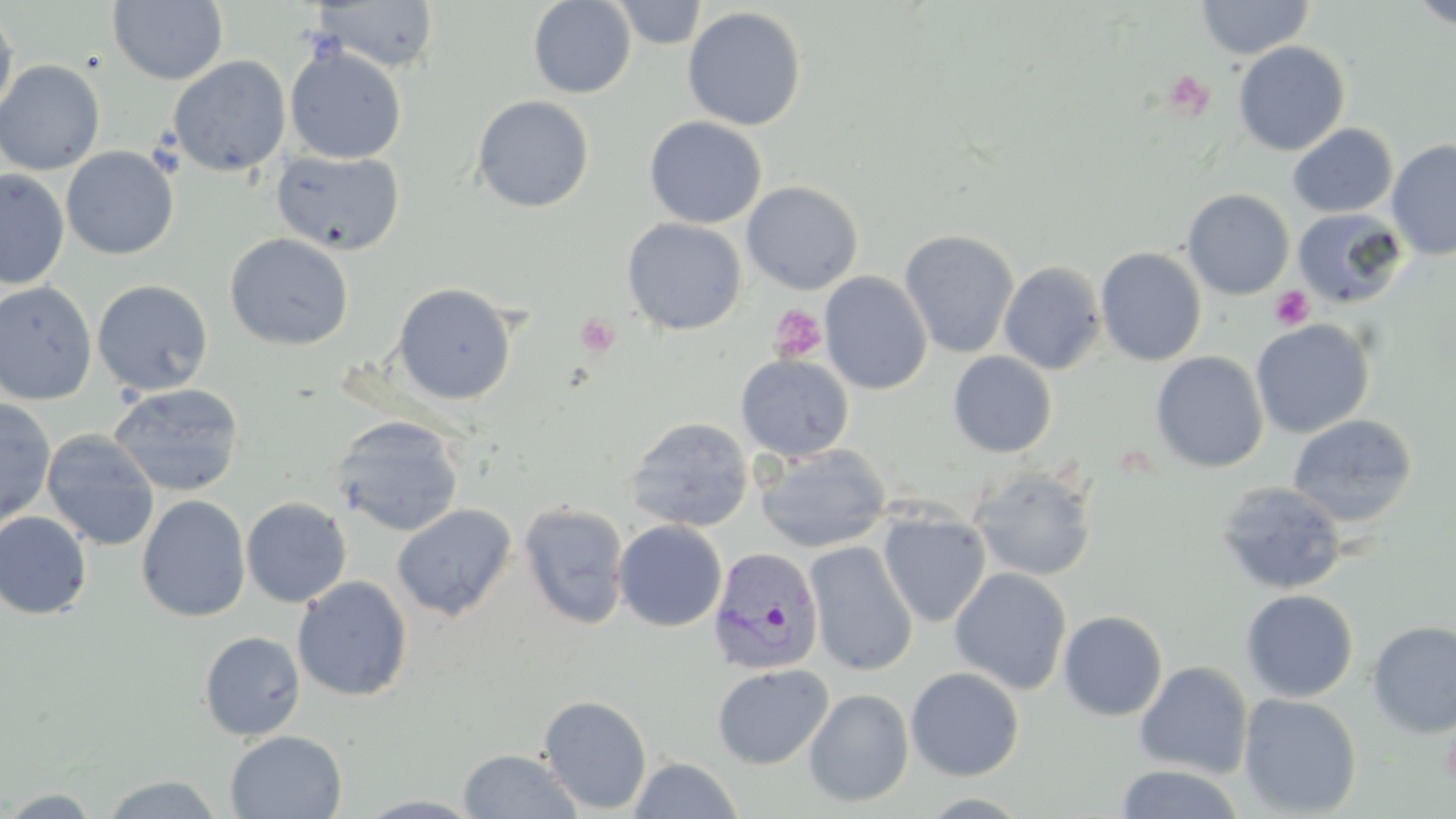
Approximate bounding boxes as [x1, y1, x2, y2] in pixels. Plasmodium vivax-infected red blood cell locations: [707, 546, 824, 675]. Uninfected red blood cell locations: [611, 0, 708, 49], [1195, 0, 1313, 59], [1407, 0, 1456, 31], [107, 1, 229, 85], [311, 1, 440, 74], [528, 1, 636, 98], [0, 5, 18, 123], [683, 6, 806, 131], [1232, 41, 1350, 156], [285, 45, 407, 164], [168, 56, 291, 177], [0, 59, 105, 175], [471, 95, 594, 213], [644, 116, 767, 228], [1287, 123, 1397, 218], [1386, 139, 1456, 261], [61, 146, 179, 260], [271, 149, 405, 256], [0, 169, 69, 289], [741, 180, 864, 295], [1182, 189, 1295, 300], [1292, 208, 1408, 308], [621, 218, 747, 335], [899, 229, 1019, 359], [224, 233, 354, 351], [1095, 246, 1207, 366], [999, 262, 1106, 374], [820, 271, 933, 395], [91, 279, 213, 396], [0, 281, 97, 405], [392, 282, 516, 405], [1250, 319, 1375, 438], [948, 351, 1057, 457], [1150, 351, 1268, 472], [735, 353, 855, 462], [108, 383, 246, 497], [0, 399, 56, 528], [1287, 414, 1418, 527], [331, 415, 465, 537], [624, 416, 755, 533], [41, 430, 160, 551], [755, 443, 891, 553], [968, 466, 1098, 582], [1215, 481, 1349, 595], [136, 494, 251, 622], [241, 497, 352, 608], [518, 502, 630, 629], [392, 503, 516, 621], [878, 509, 991, 627], [0, 511, 93, 620], [613, 520, 727, 632], [805, 540, 918, 676], [949, 567, 1072, 694], [292, 576, 413, 702], [1240, 589, 1358, 702], [1058, 610, 1168, 721], [1367, 621, 1456, 738], [199, 631, 306, 741], [1134, 661, 1253, 779], [712, 663, 833, 769], [905, 666, 1024, 781], [804, 688, 914, 807], [1237, 693, 1362, 818], [538, 695, 652, 814], [225, 730, 347, 818], [457, 748, 583, 819], [629, 756, 743, 818], [1113, 764, 1244, 819], [99, 774, 225, 818], [0, 787, 106, 817], [353, 795, 488, 818]. Platelet locations: [1163, 70, 1215, 121], [1270, 286, 1313, 330], [770, 304, 828, 363], [575, 313, 620, 358], [1441, 723, 1456, 786]. Slide-level diagnosis: Plasmodium vivax. One field of a larger specimen. Image is 1456×819 pixels. Light microscopy. Thin blood smear. 1000x magnification. May-Grünwald-Giemsa-stained preparation.